Describe the morphology of the red blood cells.
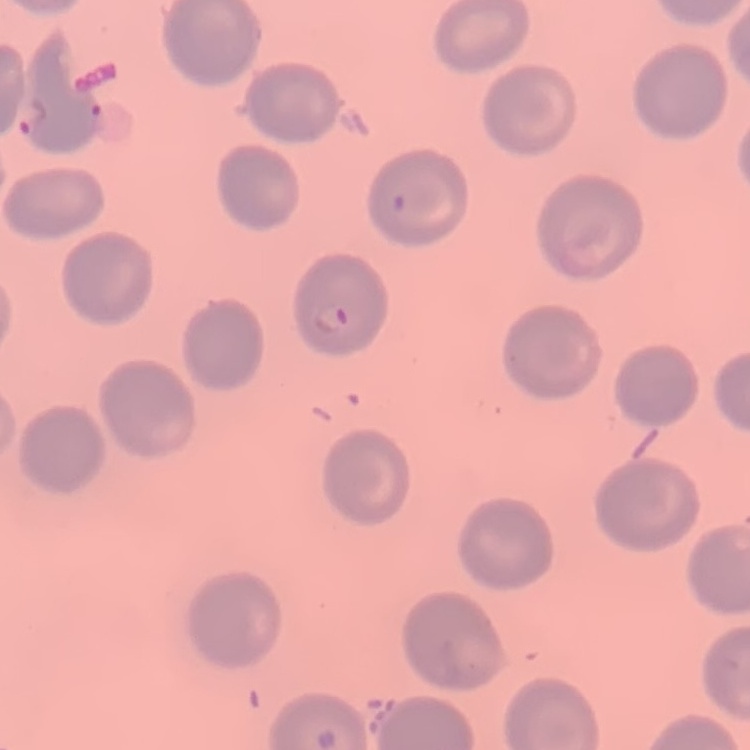
They show no rouleaux formation.

Summary:
  - Preparation: thin peripheral smear
  - Stain: Field's or Giemsa
  - Image type: one tile cut from a larger photomicrograph